Identify the cell.
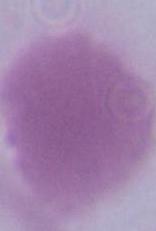
This is an erythrocyte.

Micrograph. Captured at 1000x magnification.